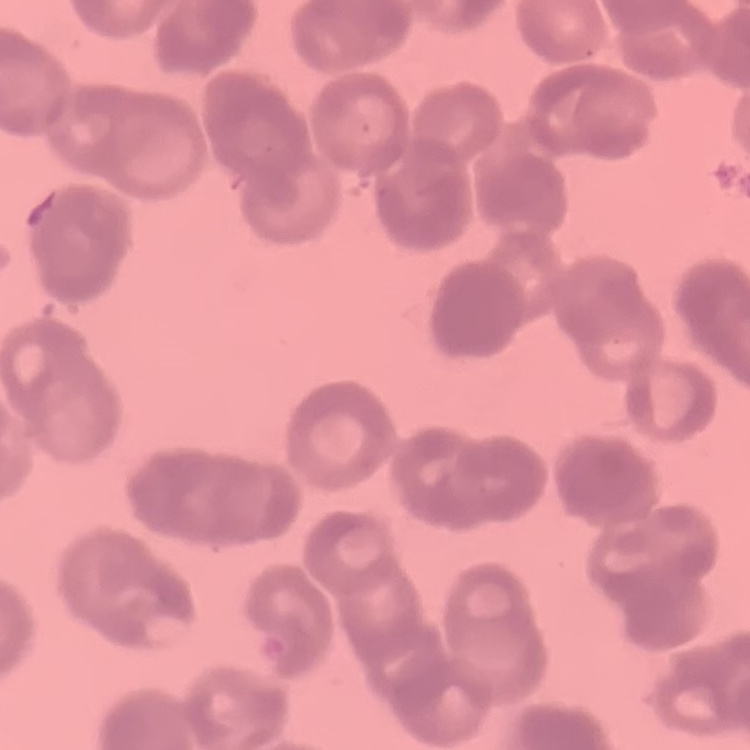

Summary:
  - Red blood cell morphology: rouleaux formation
  - Preparation: thin blood smear
  - Stain: Field's or Giemsa
  - Image type: one tile cut from a larger photomicrograph